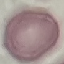

Summary:
  - Result: no malaria parasites seen
  - Image type: automatically extracted cell patch, resized to 64 × 64 pixels
  - Preparation: thin smear
  - Stain: Giemsa
  - Capture: smartphone through the microscope eyepiece